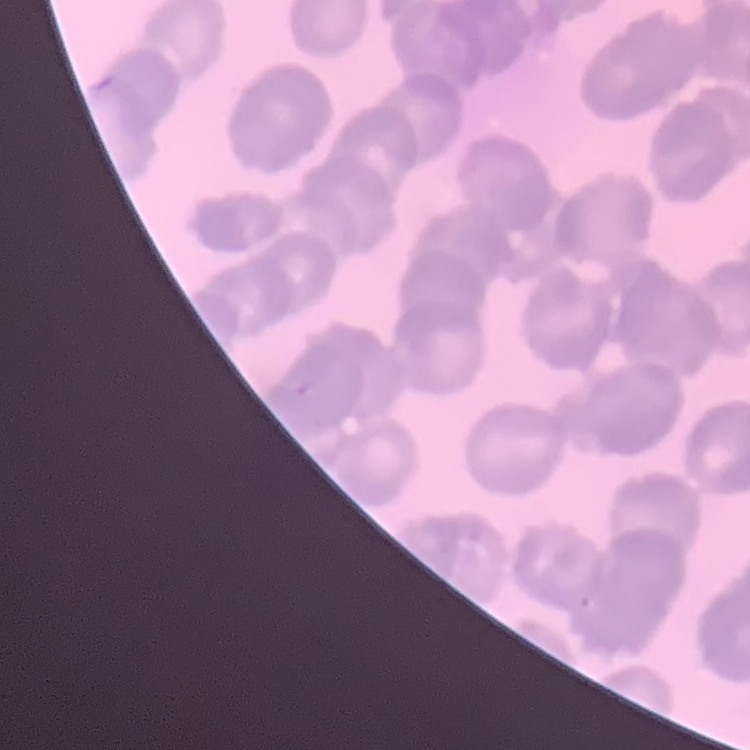
erythrocyte_morphology: rouleaux formation
preparation: thin blood film
stain: Field's or Giemsa
image_type: one tile cut from a larger photomicrograph